Comment on the morphology of the erythrocytes.
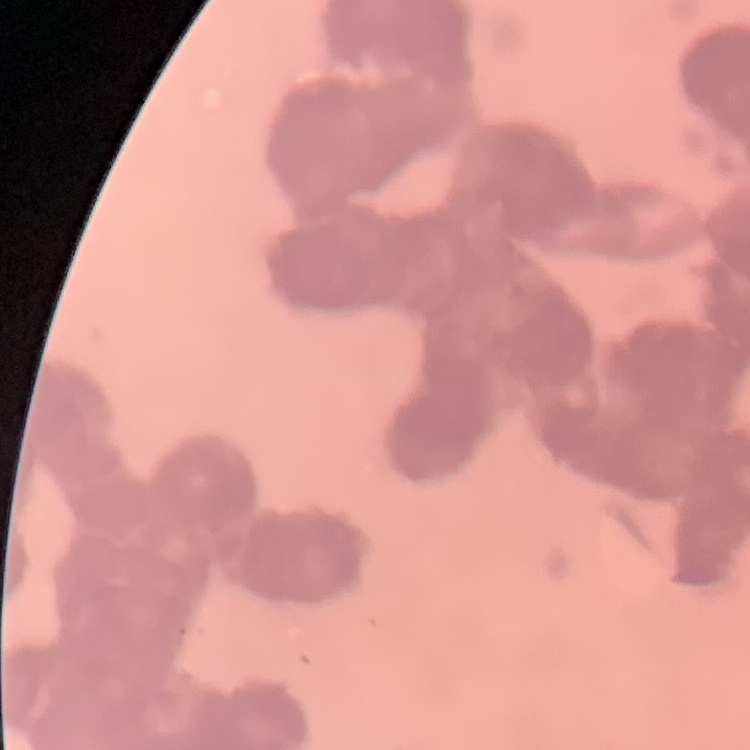
They show rouleaux formation.

Summary:
  - Image type: one tile cut from a larger photomicrograph
  - Stain: Field's or Giemsa
  - Preparation: thin peripheral smear